State which parasite is depicted.
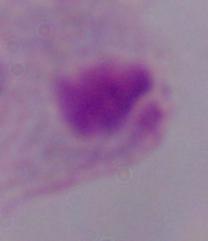
This is a trichomonad.

Summary:
  - Modality: micrograph
  - Magnification: 1000x